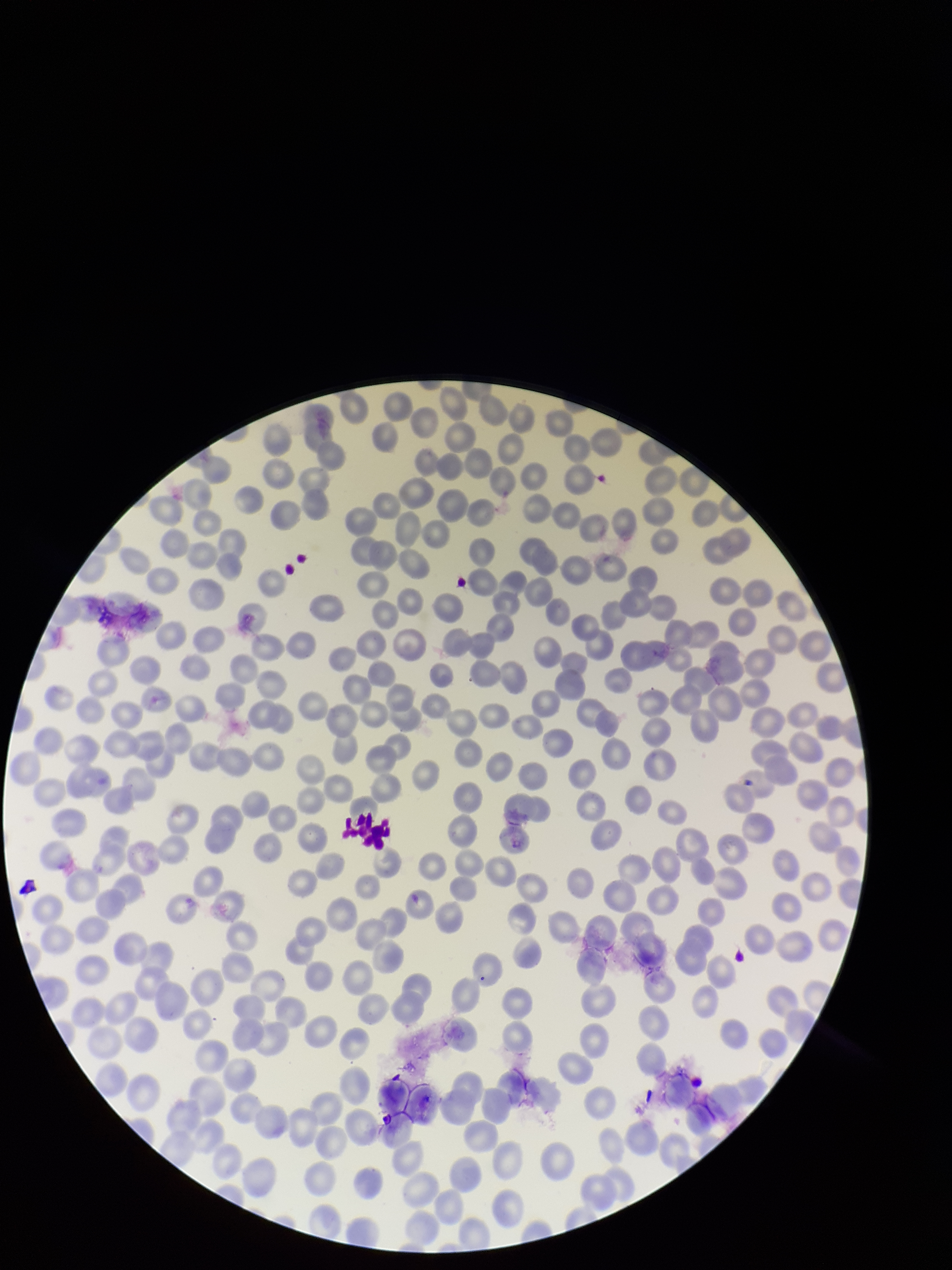
Summary:
  - Parasitized red blood cells: none seen
  - Image size: 952×1270 pixels
  - Stain: Giemsa
  - Species reported for this patient: Plasmodium falciparum
  - Patient malaria status: infected
  - Parasitized red blood cell count: 0
  - Field of view: single
  - Red blood cell count: 269
  - Preparation: thin blood smear
  - Capture: smartphone photograph through the microscope eyepiece